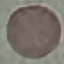
Result: no malaria parasites seen. Giemsa stain. Automatically extracted cell patch, resized to 64 × 64 pixels. Photographed with a smartphone camera at the microscope eyepiece. Thin blood smear.